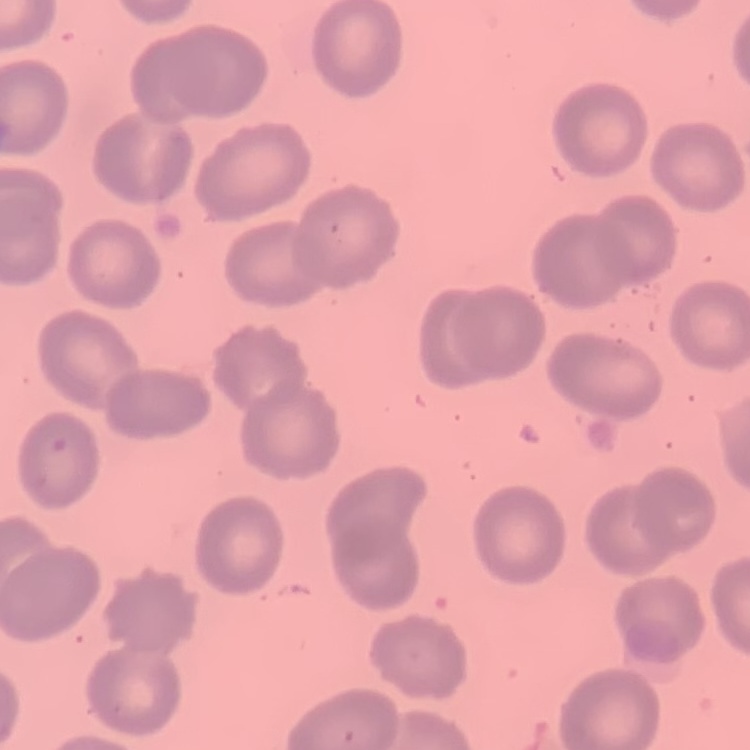 The red blood cells exhibit no rouleaux formation. Field's or Giemsa stain. One tile cut from a larger photomicrograph. Thin blood film.